Outline each Plasmodium vivax-infected red blood cell.
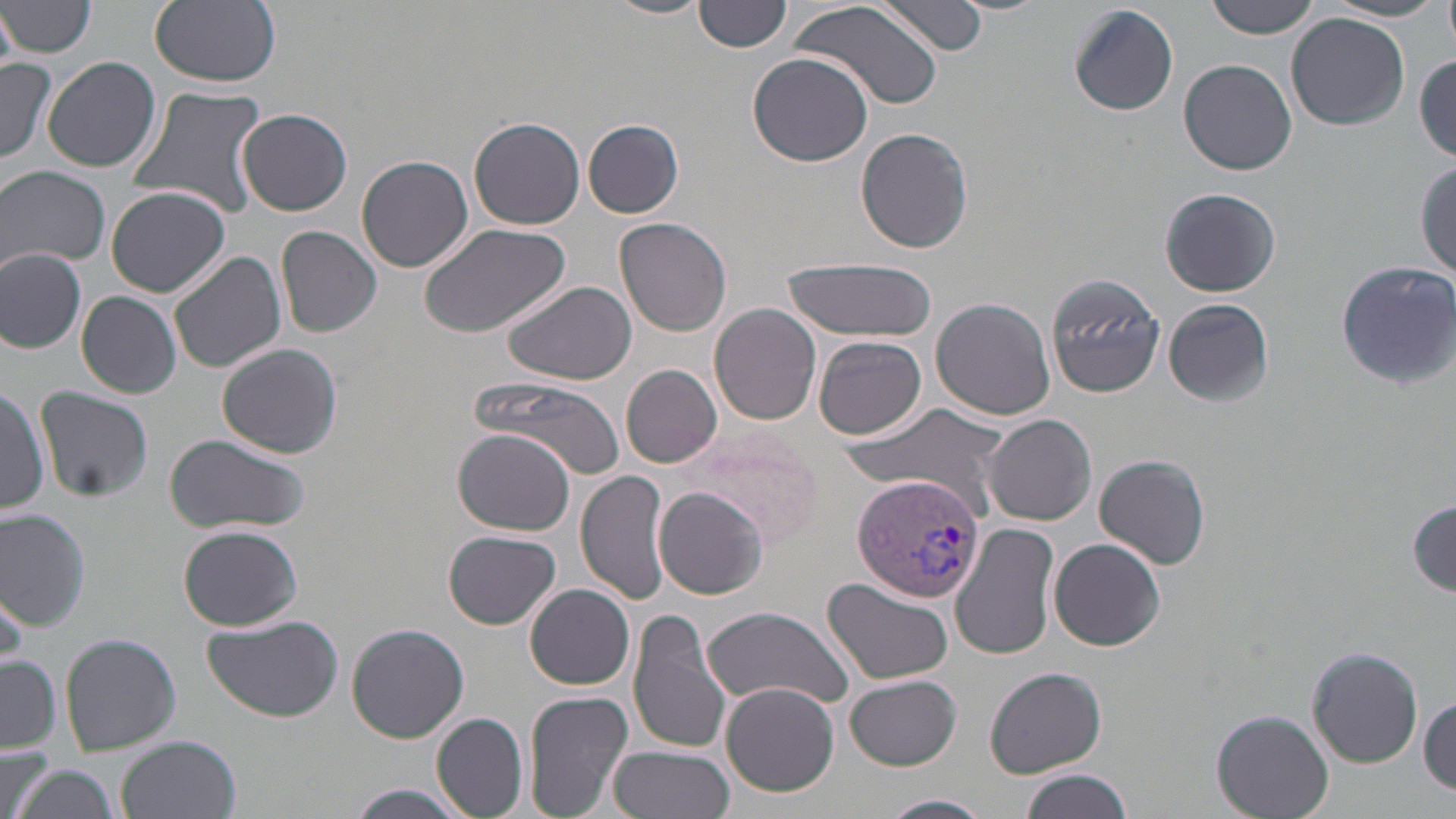

Approximate bounding boxes as (x1,y1)-(x2,y2) corner pairs in pixels.
Plasmodium vivax-infected red blood cells: (853,475)-(986,602).

Uninfected red blood cell locations: (149,0)-(282,87), (605,0)-(713,21), (698,0)-(790,53), (789,0)-(943,114), (878,0)-(989,56), (1204,0)-(1322,38), (1441,0)-(1456,51), (2,1)-(98,58), (1324,1)-(1445,23), (1068,4)-(1178,116), (1,7)-(20,71), (1287,13)-(1410,131), (747,52)-(872,166), (1414,55)-(1456,160), (42,56)-(161,173), (1,57)-(57,162), (1178,59)-(1296,175), (122,86)-(266,221), (236,109)-(353,216), (470,117)-(585,230), (582,119)-(685,219), (855,128)-(974,254), (356,154)-(473,274), (1415,163)-(1456,277), (1,167)-(112,270), (1161,185)-(1281,296), (106,186)-(230,297), (615,217)-(734,336), (419,224)-(573,339), (276,226)-(383,337), (554,242)-(715,367), (0,249)-(86,354), (169,251)-(286,373), (780,257)-(936,343), (1334,260)-(1456,390), (1044,270)-(1165,398), (499,278)-(637,384), (77,291)-(181,399), (931,298)-(1056,422), (1164,298)-(1272,406), (709,303)-(822,425), (815,336)-(927,439), (218,343)-(341,459), (621,365)-(722,467), (468,376)-(628,479), (0,381)-(48,518), (35,387)-(152,503), (835,401)-(1016,519), (983,414)-(1097,526), (672,426)-(825,552), (451,428)-(578,536), (162,433)-(310,534), (1095,454)-(1210,569), (576,469)-(676,606), (654,486)-(771,600), (1408,500)-(1456,593), (0,508)-(91,630), (951,523)-(1059,659), (179,524)-(303,631), (444,531)-(561,630), (1048,538)-(1166,650), (821,578)-(954,685), (0,581)-(26,675), (526,584)-(636,690), (698,604)-(853,710), (627,608)-(732,756), (202,617)-(341,723), (347,623)-(470,744), (60,633)-(181,755), (1307,646)-(1424,767), (1,657)-(61,753), (986,666)-(1107,777), (845,675)-(961,771), (719,683)-(841,797), (522,689)-(634,818), (1419,695)-(1456,795), (1212,710)-(1332,818), (430,712)-(529,817), (118,735)-(242,819), (1,745)-(53,819), (607,745)-(733,819), (13,761)-(121,819), (1017,768)-(1133,819), (344,785)-(474,819), (878,794)-(994,819). Slide-level diagnosis: Plasmodium vivax. One field of a larger specimen. Image is 1456×819 pixels. Thin blood film. 1000x magnification. Light microscopy. May-Grünwald-Giemsa-stained preparation.